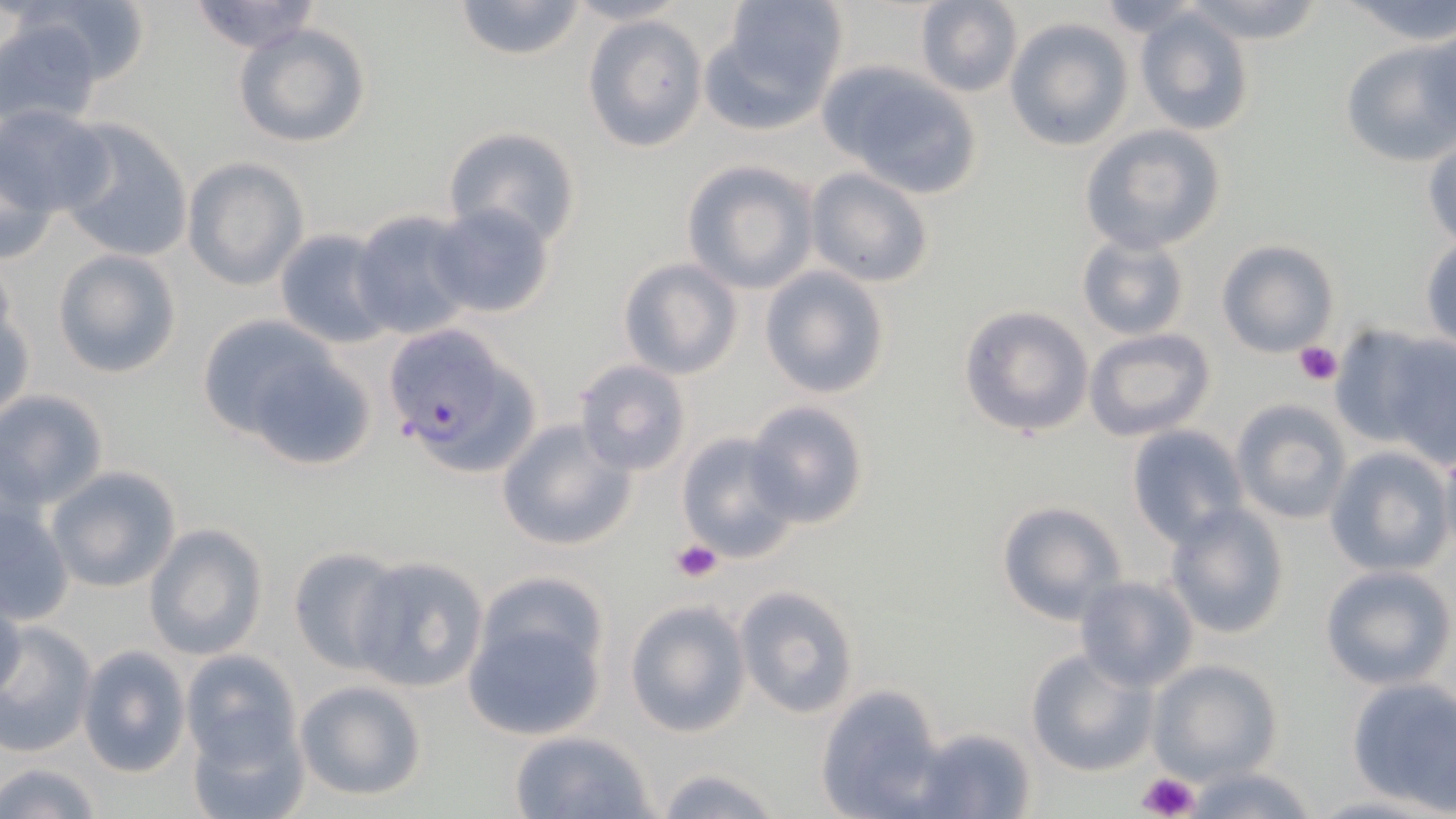
Approximate bounding boxes as (x1, y1, x2, y2) in pixels. Platelet locations: (1294, 342, 1343, 387), (671, 540, 721, 584), (1137, 770, 1201, 819). Uninfected red blood cell locations: (22, 0, 156, 94), (453, 0, 586, 62), (710, 0, 849, 124), (914, 0, 1022, 96), (1178, 0, 1327, 44), (1336, 0, 1456, 43), (184, 1, 326, 54), (565, 1, 688, 26), (1084, 2, 1215, 37), (0, 8, 116, 124), (1133, 8, 1257, 136), (583, 14, 709, 154), (1004, 17, 1133, 151), (233, 22, 371, 149), (1413, 28, 1456, 148), (1340, 38, 1456, 164), (823, 64, 984, 196), (1, 104, 115, 220), (54, 119, 195, 266), (1080, 125, 1227, 255), (443, 126, 582, 249), (1424, 135, 1456, 250), (2, 141, 60, 268), (183, 158, 308, 290), (683, 161, 818, 294), (805, 165, 935, 289), (429, 203, 555, 320), (351, 208, 478, 341), (274, 228, 393, 347), (1076, 233, 1191, 342), (1421, 237, 1455, 351), (1214, 238, 1340, 359), (52, 249, 182, 379), (617, 258, 743, 380), (759, 266, 892, 399), (1, 301, 34, 423), (957, 305, 1094, 439), (196, 314, 342, 442), (1329, 321, 1452, 454), (1083, 328, 1216, 442), (1386, 337, 1456, 471), (231, 343, 378, 474), (573, 358, 693, 475), (0, 388, 108, 510), (1231, 398, 1352, 525), (746, 400, 870, 529), (497, 418, 635, 552), (1127, 424, 1248, 546), (676, 431, 799, 561), (1325, 446, 1453, 577), (1437, 446, 1456, 559), (46, 465, 182, 591), (994, 498, 1127, 625), (1164, 503, 1291, 640), (0, 505, 75, 625), (143, 523, 270, 662), (287, 548, 403, 673), (352, 556, 489, 694), (1319, 564, 1454, 689), (1075, 575, 1198, 691), (734, 584, 860, 720), (0, 591, 26, 704), (622, 598, 753, 739), (463, 599, 609, 742), (0, 621, 97, 758), (76, 646, 190, 777), (180, 648, 300, 783), (1025, 649, 1157, 777), (1148, 659, 1282, 784), (1347, 677, 1456, 811), (293, 678, 429, 804), (815, 685, 947, 819), (182, 706, 309, 819), (908, 726, 1036, 818), (508, 728, 659, 819), (1, 759, 103, 819), (650, 764, 785, 819), (1180, 764, 1320, 819). Plasmodium falciparum-infected red blood cell locations: (381, 322, 542, 478). Slide-level diagnosis: Plasmodium falciparum. 1000x magnification. May-Grünwald-Giemsa-stained preparation. Image is 1456×819 pixels. Light microscopy. One field of a larger specimen. Thin blood film.